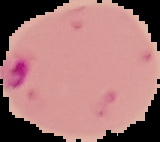

preparation = thin blood film
image size = 160×142 pixels
result = Plasmodium parasites detected
image type = cell region segmented out of the field of view; surrounding area masked to black